Locate every Plasmodium falciparum-infected red blood cell.
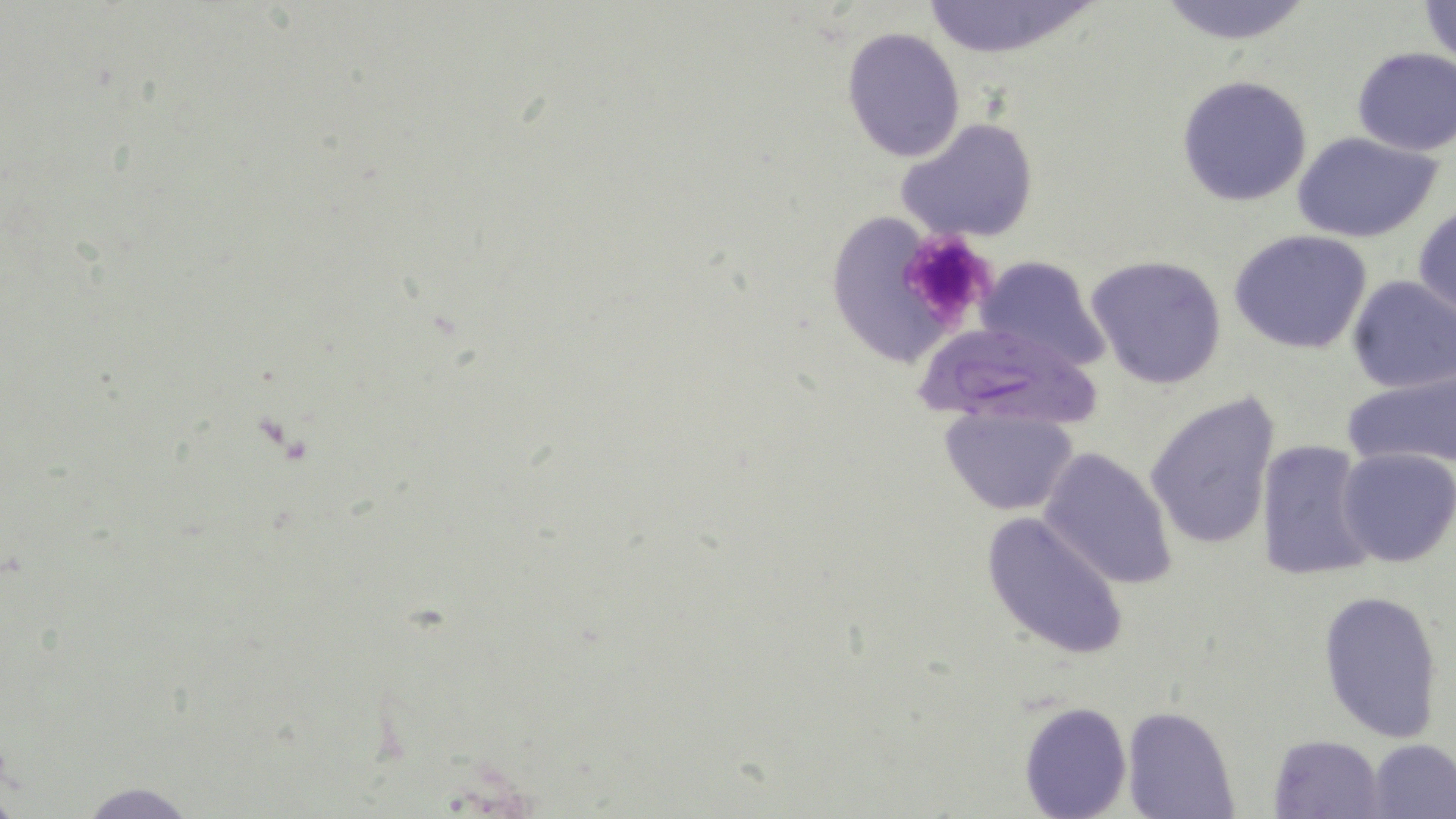
Approximate bounding boxes as named x1/y1/x2/y2 corners in pixels.
Plasmodium falciparum-infected red blood cells: (x1=916, y1=328, x2=1106, y2=437).

slide-level diagnosis = Plasmodium falciparum
platelet locations = approximate bounding boxes as named x1/y1/x2/y2 corners in pixels: (x1=896, y1=230, x2=997, y2=329)
image size = 1456×819 pixels
modality = light microscopy
preparation = thin blood film
uninfected red blood cell locations = approximate bounding boxes as named x1/y1/x2/y2 corners in pixels: (x1=1155, y1=0, x2=1316, y2=46), (x1=1418, y1=0, x2=1456, y2=64), (x1=919, y1=1, x2=1099, y2=59), (x1=841, y1=27, x2=965, y2=162), (x1=1351, y1=46, x2=1456, y2=156), (x1=1175, y1=75, x2=1313, y2=207), (x1=897, y1=117, x2=1039, y2=243), (x1=1291, y1=130, x2=1446, y2=242), (x1=1414, y1=203, x2=1456, y2=322), (x1=839, y1=212, x2=950, y2=367), (x1=1229, y1=228, x2=1374, y2=355), (x1=976, y1=255, x2=1108, y2=373), (x1=1086, y1=256, x2=1227, y2=390), (x1=1345, y1=276, x2=1456, y2=393), (x1=1341, y1=366, x2=1456, y2=473), (x1=1144, y1=392, x2=1283, y2=552), (x1=940, y1=406, x2=1077, y2=516), (x1=1257, y1=439, x2=1379, y2=583), (x1=1039, y1=445, x2=1177, y2=590), (x1=1337, y1=447, x2=1456, y2=567), (x1=980, y1=509, x2=1130, y2=662), (x1=1317, y1=590, x2=1445, y2=744), (x1=1019, y1=700, x2=1132, y2=818), (x1=1123, y1=707, x2=1238, y2=819), (x1=1268, y1=733, x2=1384, y2=818), (x1=1365, y1=738, x2=1456, y2=817), (x1=72, y1=781, x2=201, y2=817)
field of view = single
stain = May-Grünwald-Giemsa
magnification = 1000x